Identify the cell.
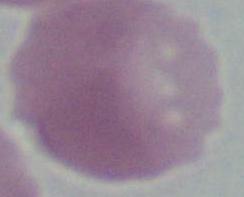

This is an erythrocyte.

{
  "modality": "micrograph",
  "magnification": "1000x"
}